State which parasite is depicted.
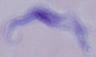
A trypanosome.

Captured at 1000x magnification. Photomicrograph.